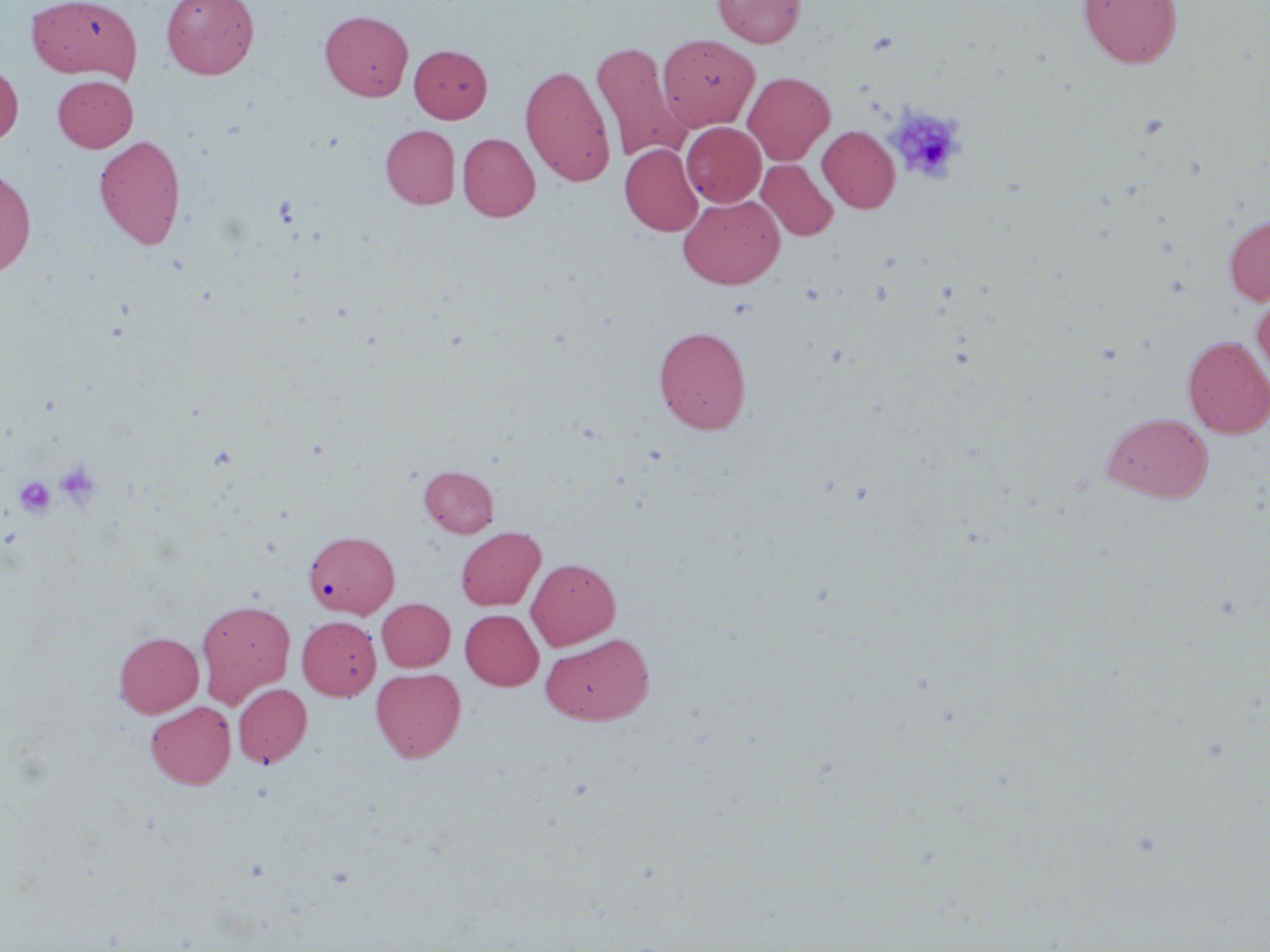

Summary:
  - Coordinate format: approximate bounding boxes as (x1,y1)-(x2,y2) corner pairs in pixels
  - Uninfected red blood cell locations: (28,0)-(142,81), (161,0)-(259,79), (713,0)-(806,48), (1078,0)-(1182,67), (320,10)-(413,101), (657,34)-(760,132), (590,41)-(691,163), (409,45)-(492,123), (0,63)-(23,146), (520,64)-(616,185), (743,72)-(835,165), (53,75)-(138,151), (681,122)-(766,207), (381,125)-(460,208), (818,126)-(900,213), (458,133)-(540,222), (94,135)-(186,249), (620,143)-(703,236), (757,159)-(838,241), (0,169)-(36,276), (678,194)-(785,289), (1223,213)-(1270,306), (1251,290)-(1270,386), (653,325)-(751,434), (1183,336)-(1270,438), (1102,412)-(1213,502), (419,464)-(499,537), (456,526)-(545,610), (304,529)-(400,619), (526,557)-(620,649), (376,598)-(455,671), (195,599)-(296,706), (460,609)-(544,690), (297,615)-(381,701), (114,632)-(204,717), (540,632)-(655,725), (371,667)-(466,762), (233,683)-(312,767), (146,701)-(236,789)
  - Platelet locations: (888,107)-(965,183), (55,461)-(103,509), (15,476)-(56,518)
  - Slide-level diagnosis: no evidence of blood parasites
  - Preparation: thin blood film
  - Modality: light microscopy
  - Field of view: one of a larger specimen
  - Stain: May-Grünwald-Giemsa
  - Magnification: 1000x
  - Image size: 1270×952 pixels